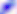

magnification = 400x
identification = Toxoplasma gondii
modality = micrograph